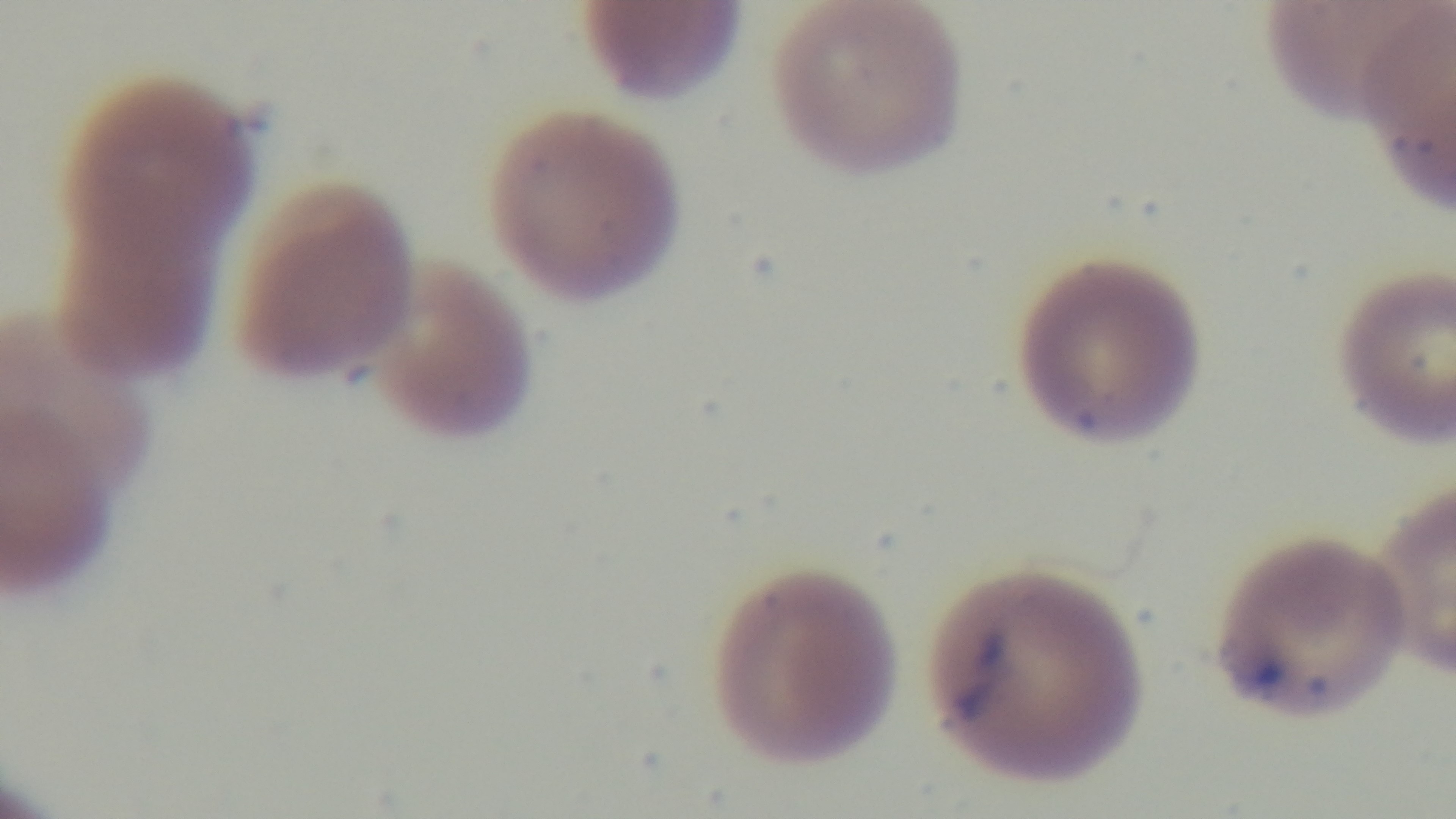

Summary:
  - Field of view: one from the slide
  - Objective: 100x oil immersion
  - Modality: light microscopy
  - Preparation: thin
  - Malaria status: positive
  - Stain: Giemsa
  - Capture: mounted 4K digital camera